Classify this cell by malaria status.
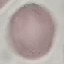
Uninfected.

image type = automatically extracted cell patch, resized to 64 × 64 pixels
capture = smartphone camera at the microscope eyepiece
stain = Giemsa
preparation = thin smear